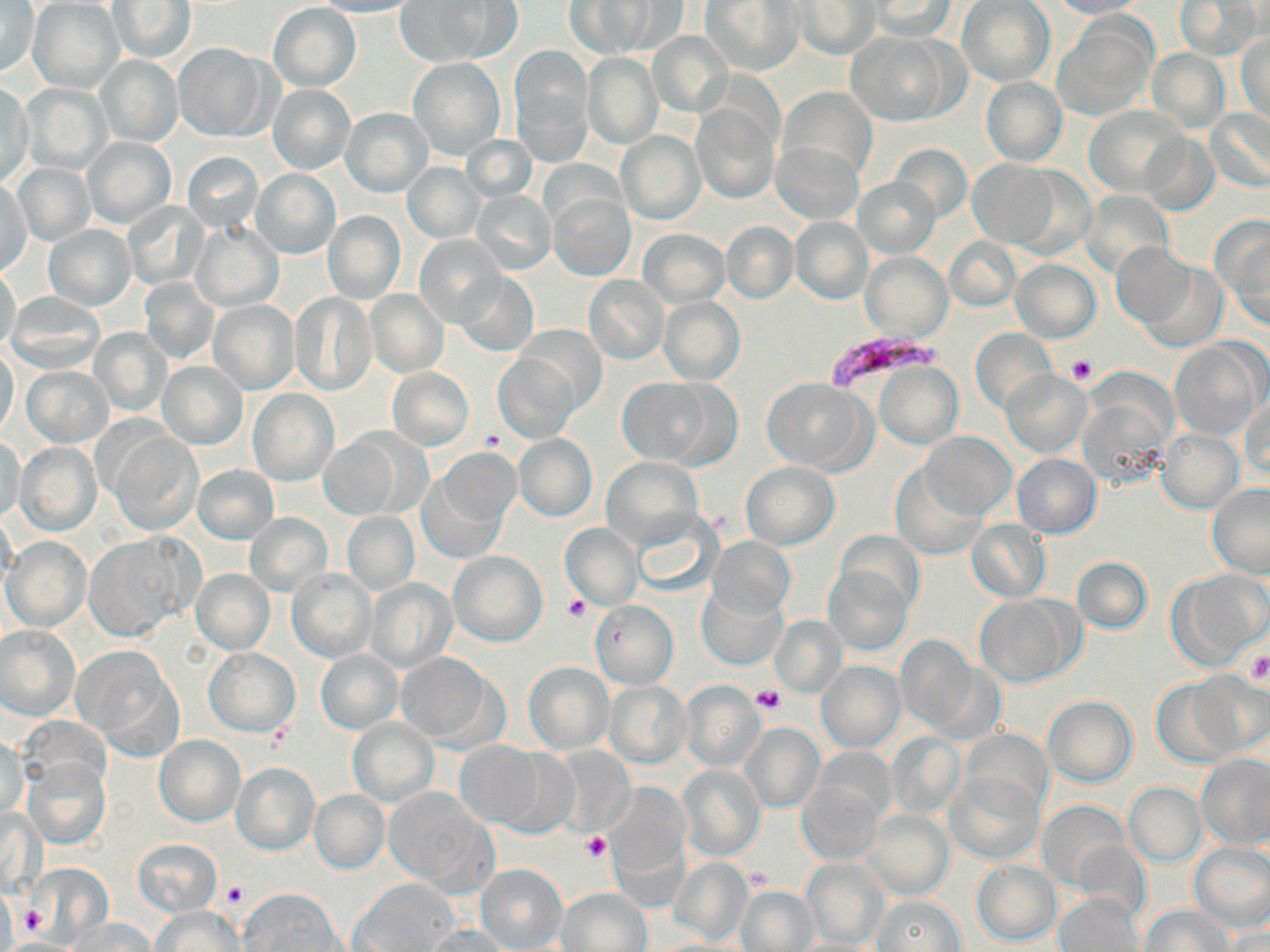
Summary:
  - Coordinate format: approximate bounding boxes as [x1, y1, x2, y2] in pixels
  - Plasmodium falciparum-infected red blood cell locations: [824, 330, 948, 392]
  - Uninfected red blood cell locations: [316, 0, 424, 18], [1175, 0, 1262, 60], [27, 1, 123, 92], [396, 1, 516, 67], [565, 1, 657, 58], [702, 1, 803, 75], [867, 1, 959, 39], [957, 1, 1054, 86], [1048, 1, 1149, 19], [0, 2, 39, 77], [106, 2, 197, 63], [794, 2, 878, 59], [268, 3, 361, 91], [1054, 17, 1154, 119], [646, 31, 734, 119], [1237, 31, 1270, 123], [846, 32, 954, 125], [173, 44, 273, 142], [511, 47, 593, 161], [1145, 50, 1229, 132], [582, 52, 663, 150], [96, 55, 183, 146], [407, 58, 504, 159], [981, 76, 1066, 166], [1, 81, 34, 190], [22, 83, 112, 175], [267, 85, 357, 175], [779, 87, 878, 181], [1084, 106, 1184, 195], [341, 107, 433, 196], [692, 108, 779, 203], [1206, 108, 1269, 192], [1149, 118, 1269, 205], [615, 131, 704, 225], [1139, 133, 1219, 215], [82, 136, 176, 230], [464, 136, 537, 204], [772, 142, 861, 224], [891, 144, 971, 222], [182, 151, 263, 233], [967, 159, 1060, 248], [402, 163, 485, 244], [13, 164, 96, 246], [252, 169, 339, 258], [0, 178, 33, 280], [855, 178, 937, 256], [1081, 190, 1174, 278], [471, 191, 556, 276], [548, 193, 634, 280], [122, 202, 207, 290], [323, 210, 405, 303], [1213, 216, 1270, 326], [791, 217, 872, 302], [721, 221, 798, 303], [193, 223, 283, 311], [44, 224, 135, 310], [640, 229, 729, 307], [416, 233, 508, 328], [944, 236, 1020, 311], [1111, 242, 1194, 326], [862, 252, 953, 342], [1009, 258, 1100, 342], [1140, 261, 1229, 352], [0, 265, 21, 354], [455, 270, 538, 357], [583, 275, 669, 365], [139, 278, 218, 364], [365, 290, 449, 377], [290, 291, 379, 396], [5, 293, 104, 372], [658, 296, 744, 384], [208, 300, 300, 394], [515, 324, 604, 417], [90, 328, 170, 416], [971, 329, 1056, 415], [1168, 339, 1262, 441], [0, 348, 21, 440], [494, 353, 579, 443], [874, 360, 962, 449], [159, 361, 248, 449], [22, 365, 113, 445], [389, 368, 473, 449], [1002, 370, 1091, 458], [760, 377, 877, 474], [619, 378, 718, 467], [248, 389, 338, 484], [1081, 395, 1170, 489], [1240, 395, 1269, 484], [110, 430, 203, 536], [1156, 430, 1242, 512], [921, 432, 1015, 518], [320, 434, 404, 519], [515, 434, 596, 520], [1, 435, 26, 525], [16, 442, 101, 535], [1012, 454, 1101, 538], [424, 455, 514, 558], [602, 456, 704, 551], [739, 461, 839, 550], [194, 465, 278, 543], [891, 465, 986, 559], [1207, 483, 1270, 577], [631, 510, 723, 597], [343, 512, 418, 594], [245, 513, 332, 597], [966, 520, 1050, 601], [560, 522, 643, 610], [835, 530, 924, 614], [85, 534, 197, 640], [3, 535, 90, 631], [708, 536, 795, 620], [449, 551, 547, 646], [1072, 556, 1152, 634], [824, 565, 912, 654], [192, 568, 275, 654], [289, 569, 375, 662], [1178, 569, 1269, 662], [367, 577, 459, 673], [699, 588, 786, 668], [975, 594, 1078, 687], [590, 600, 678, 689], [770, 614, 847, 697], [0, 625, 81, 720], [895, 636, 980, 735], [73, 645, 180, 752], [203, 646, 300, 737], [317, 650, 402, 733], [395, 653, 500, 747], [816, 659, 905, 753], [522, 660, 614, 754], [1186, 672, 1269, 756], [1152, 677, 1241, 766], [606, 682, 691, 767], [680, 682, 766, 771], [1043, 695, 1136, 786], [348, 718, 438, 805], [740, 723, 824, 812], [960, 728, 1051, 813], [886, 733, 965, 820], [1, 735, 27, 820], [154, 736, 245, 825], [455, 740, 545, 828], [548, 746, 635, 835], [816, 746, 895, 824], [500, 751, 582, 839], [1198, 753, 1270, 848], [22, 758, 110, 850], [231, 762, 320, 855], [676, 764, 765, 861], [945, 772, 1041, 862], [796, 779, 882, 865], [606, 782, 689, 877], [1124, 784, 1205, 866], [309, 788, 390, 874], [381, 788, 490, 890], [1038, 800, 1130, 892], [863, 811, 954, 899], [133, 838, 222, 915], [1070, 838, 1152, 925], [1190, 843, 1270, 931], [668, 856, 753, 945], [803, 857, 889, 949], [971, 859, 1061, 946], [30, 863, 113, 948], [477, 864, 567, 950], [349, 880, 458, 952], [736, 884, 818, 952], [557, 886, 651, 951], [240, 888, 344, 951], [1055, 892, 1145, 952], [871, 896, 966, 951], [151, 905, 243, 952], [1140, 905, 1234, 952], [70, 917, 155, 951], [424, 924, 513, 952], [1222, 928, 1270, 952], [788, 938, 886, 952]
  - Platelet locations: [1066, 354, 1098, 387], [481, 428, 509, 451], [562, 596, 590, 622], [1244, 653, 1270, 685], [752, 686, 783, 716], [581, 832, 612, 860], [747, 865, 773, 890], [221, 881, 246, 907], [20, 904, 49, 937]
  - Slide-level diagnosis: Plasmodium falciparum
  - Preparation: thin blood film
  - Magnification: 1000x
  - Modality: optical microscopy
  - Field of view: single
  - Stain: May-Grünwald-Giemsa
  - Image size: 1270×952 pixels